Comment on the morphology of the red blood cells.
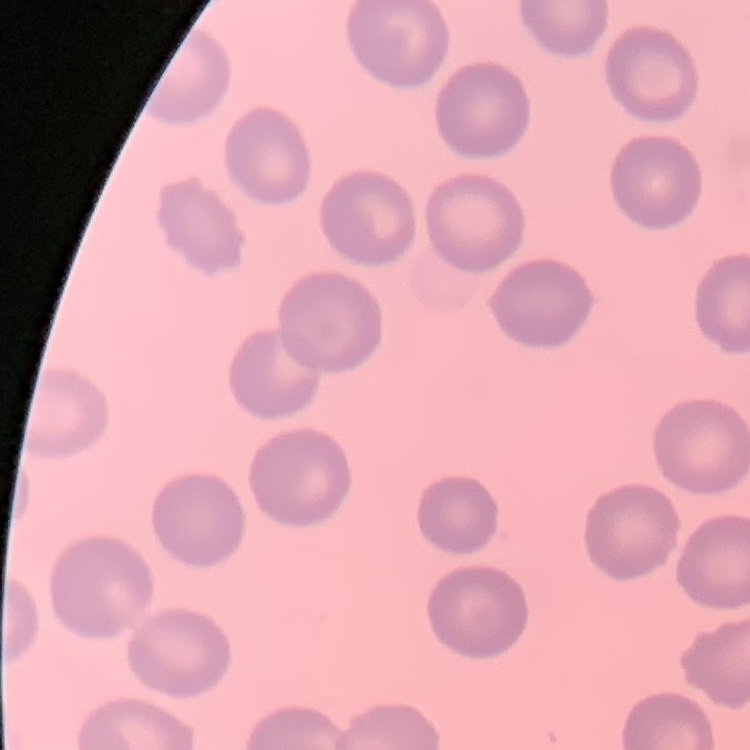

They show no rouleaux formation.

stain = Field's or Giemsa
image type = square crop of a larger photomicrograph
preparation = thin peripheral smear